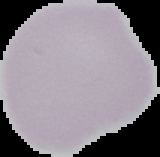

Image is 160×157 pixels. The area outside the segmented cell region is set to black. From a thin blood film. Malaria status: uninfected.